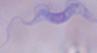 Captured at 1000x magnification. A trypanosome is seen. Micrograph.